Classify this cell by malaria status.
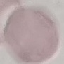
Uninfected.

preparation = thin smear
capture = smartphone camera at the microscope eyepiece
image type = cell patch, automatically extracted from a larger field of view and resized to 64 × 64 pixels
stain = Giemsa